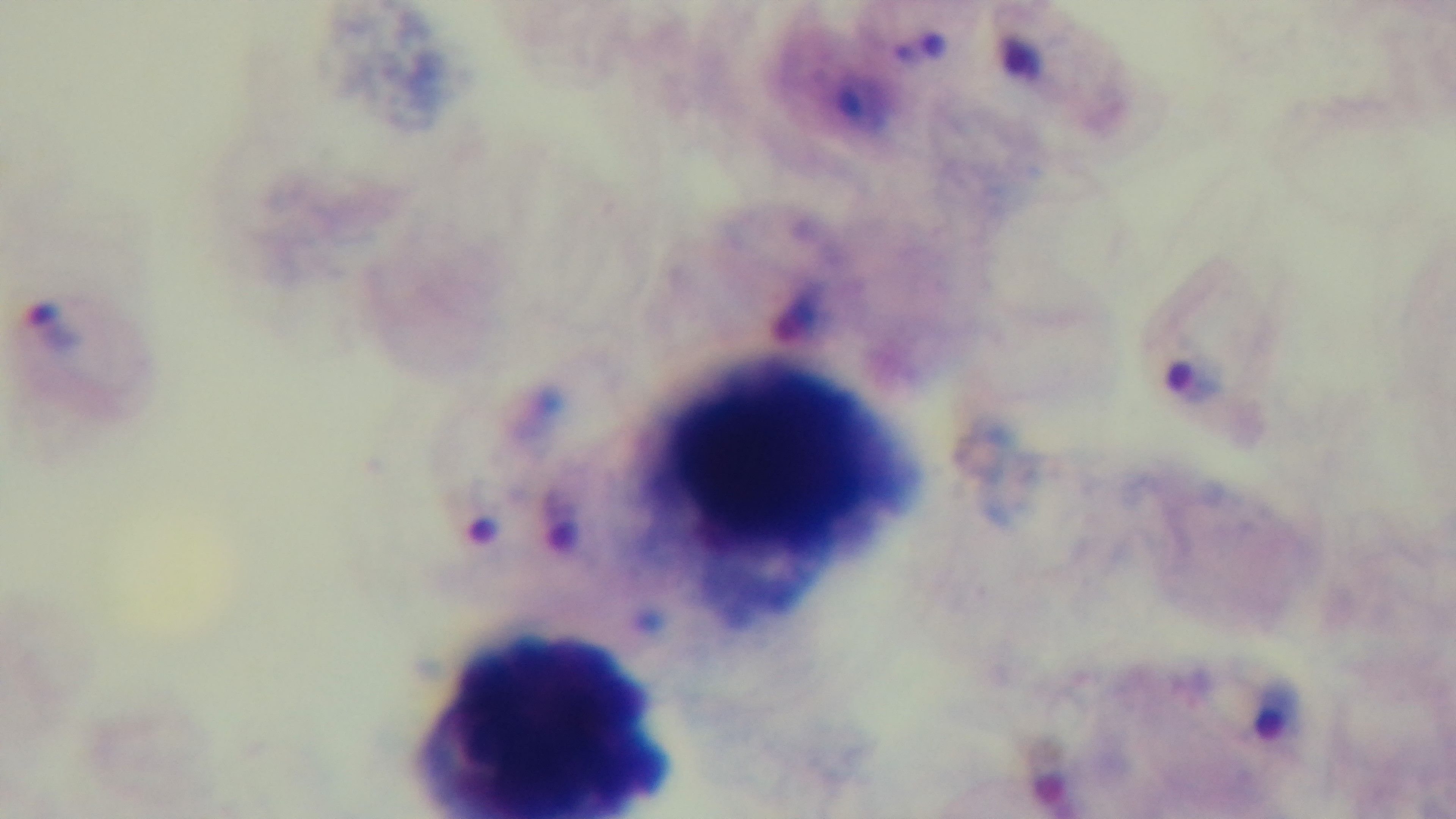

stain = Giemsa
capture = mounted 4K digital camera
malaria status = positive
objective = 100x oil immersion
modality = light microscopy
preparation = thick smear
field of view = single